Give the extent of all white blood cells.
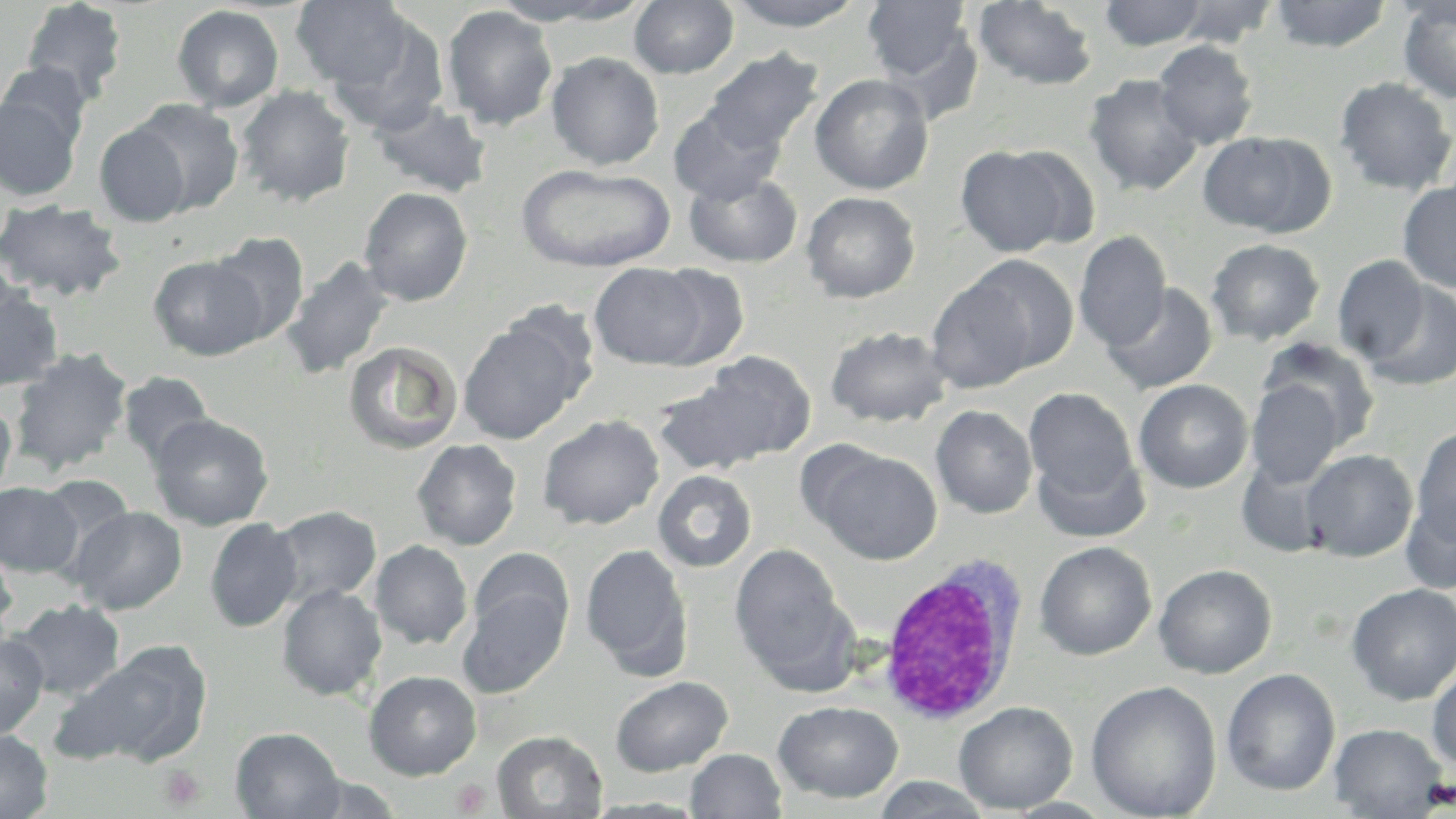
Approximate bounding boxes as [x1, y1, x2, y2] in pixels.
White blood cells: [876, 558, 1029, 728].

slide_level_diagnosis: negative for blood parasites
preparation: thin blood smear
image_size: 1456×819 pixels
uninfected_red_blood_cell_locations: 'approximate bounding boxes as [x1, y1, x2, y2] in pixels: [972, 0, 1099, 91], [1169, 0, 1281, 47], [1270, 0, 1392, 52], [1397, 0, 1456, 104], [20, 1, 128, 105], [291, 1, 414, 91], [495, 1, 648, 26], [629, 1, 738, 79], [726, 1, 868, 31], [863, 1, 975, 86], [1098, 1, 1209, 50], [172, 5, 285, 112], [441, 5, 558, 130], [326, 12, 451, 136], [1153, 40, 1259, 149], [702, 49, 824, 156], [546, 52, 665, 170], [0, 61, 94, 151], [810, 73, 934, 195], [1083, 73, 1204, 196], [1333, 76, 1455, 196], [235, 86, 356, 207], [0, 96, 82, 201], [130, 99, 244, 215], [370, 100, 493, 198], [667, 105, 785, 205], [94, 123, 192, 228], [1196, 132, 1330, 236], [954, 145, 1077, 257], [516, 163, 676, 273], [683, 170, 803, 268], [1397, 179, 1456, 293], [358, 186, 473, 307], [801, 191, 920, 303], [0, 198, 127, 302], [208, 231, 310, 345], [1074, 231, 1171, 352], [1206, 238, 1325, 346], [148, 254, 268, 361], [964, 255, 1079, 373], [1332, 255, 1431, 364], [281, 256, 395, 380], [588, 263, 712, 369], [647, 265, 750, 369], [926, 277, 1041, 393], [0, 281, 64, 392], [1360, 281, 1456, 391], [1101, 282, 1218, 395], [458, 321, 584, 445], [825, 325, 952, 428], [1257, 339, 1382, 452], [343, 341, 463, 454], [9, 347, 133, 475], [698, 352, 816, 461], [118, 371, 215, 467], [653, 376, 777, 476], [1133, 379, 1253, 493], [1246, 379, 1348, 488], [1024, 388, 1138, 501], [0, 397, 17, 501], [931, 405, 1037, 518], [148, 413, 274, 531], [537, 414, 665, 530], [1411, 426, 1456, 546], [412, 439, 522, 551], [1032, 448, 1148, 543], [1301, 448, 1418, 562], [816, 449, 942, 564], [652, 470, 757, 572], [35, 473, 136, 565], [0, 482, 81, 578], [1401, 489, 1456, 594], [268, 505, 382, 607], [68, 506, 188, 615], [204, 518, 303, 633], [0, 538, 18, 638], [370, 540, 473, 649], [1034, 541, 1157, 661], [580, 543, 692, 676], [730, 544, 848, 678], [468, 548, 572, 644], [1153, 563, 1277, 678], [1346, 583, 1456, 705], [276, 584, 387, 701], [458, 585, 570, 698], [8, 599, 126, 700], [0, 633, 49, 740], [52, 645, 212, 769], [1427, 664, 1456, 773], [1221, 668, 1340, 797], [363, 670, 483, 780], [610, 675, 733, 776], [1086, 681, 1222, 819], [773, 700, 904, 803], [954, 701, 1078, 814], [1329, 723, 1448, 817], [230, 727, 345, 818], [0, 730, 53, 818], [492, 730, 608, 819], [685, 748, 787, 818], [291, 772, 406, 818], [872, 776, 993, 817], [582, 796, 709, 817], [1004, 797, 1117, 818]'
platelet_locations: 'approximate bounding boxes as [x1, y1, x2, y2] in pixels: [158, 764, 206, 810], [451, 779, 491, 816]'
magnification: 1000x
modality: light microscopy
stain: May-Grünwald-Giemsa
field_of_view: single